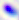

Summary:
  - Magnification: 400x
  - Modality: photomicrograph
  - Identification: Toxoplasma gondii